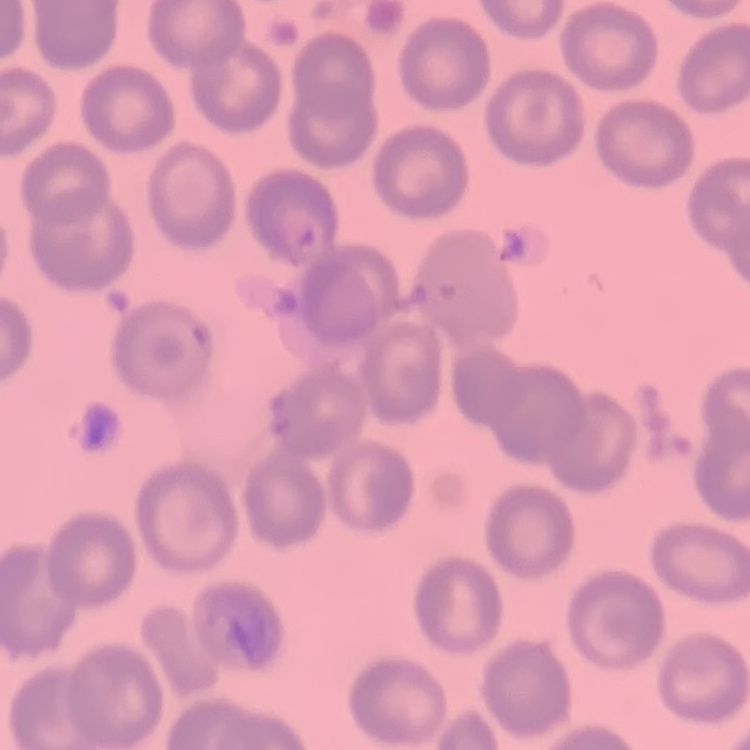
Summary:
  - Erythrocyte morphology: no rouleaux formation
  - Preparation: thin peripheral smear
  - Image type: one tile cut from a larger photomicrograph
  - Stain: Field's or Giemsa